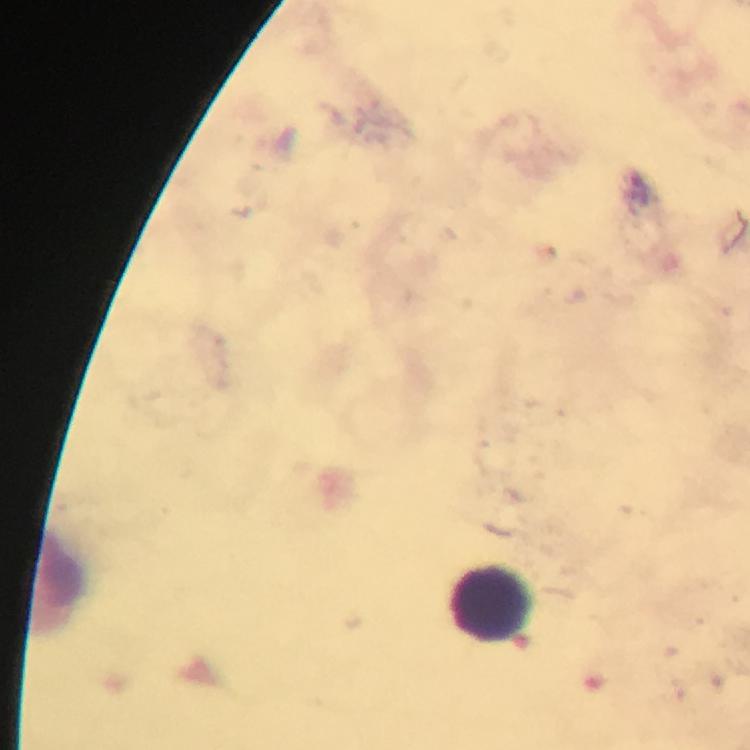

Approximate centers as (x, y) in pixels.
Summary:
  - Leukocyte locations: (490, 605)
  - Capture: smartphone camera through the microscope
  - Plasmodium parasites: none detected
  - Immersion oil: applied
  - Stain: Giemsa
  - Context: from a diagnostic examination for malaria
  - Preparation: thick smear
  - Cropped from: a single field of view
  - Image size: 750×750 pixels
  - Magnification: 100x